Classify this cell by malaria status.
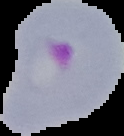
Parasitized.

Segmented cell region on a black background. Image is 124×136 pixels. From a thin blood film.